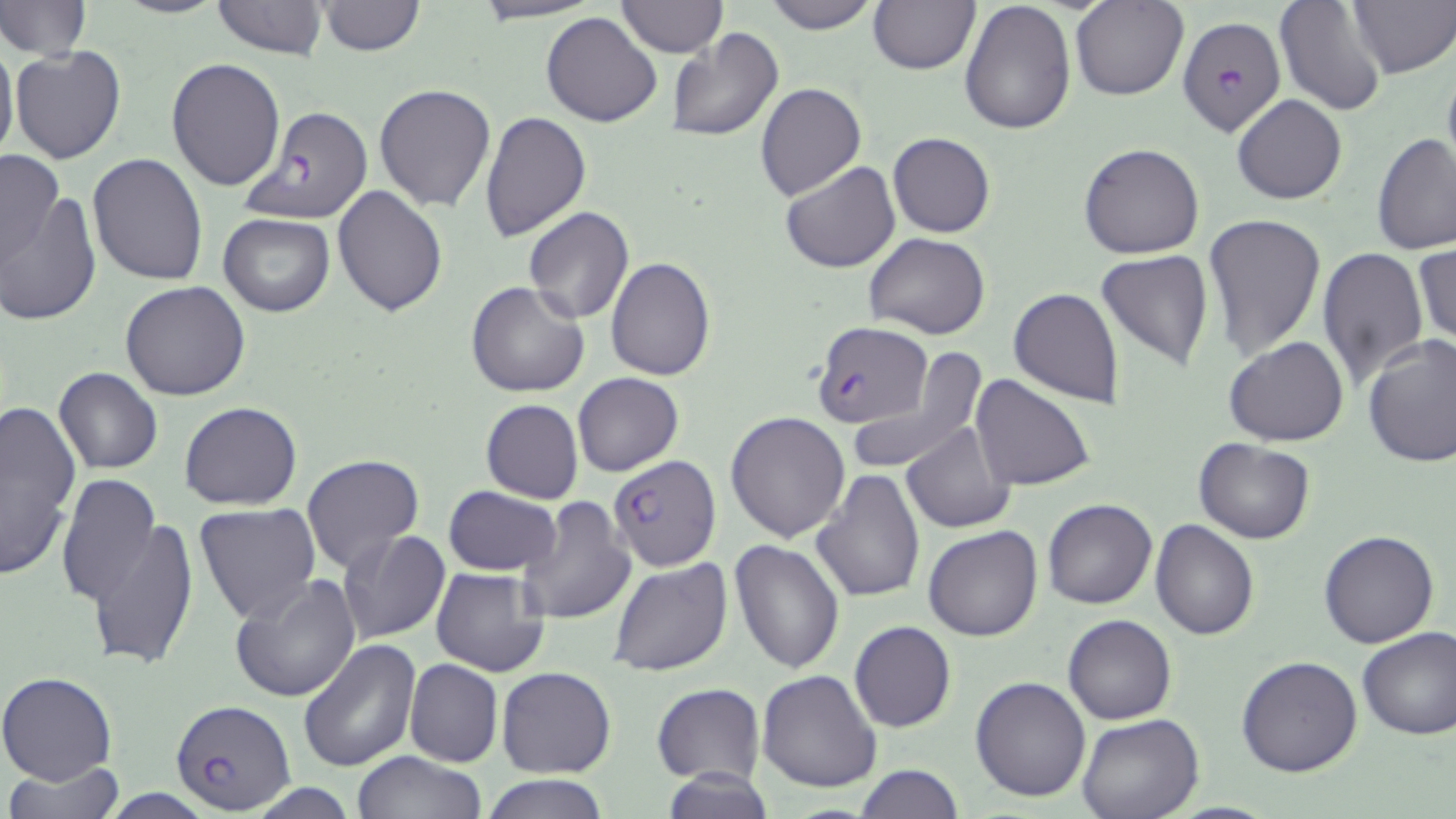
Approximate bounding boxes as named x1/y1/x2/y2 corners in pixels. Uninfected red blood cell locations: (x1=113, y1=0, x2=226, y2=20), (x1=210, y1=0, x2=329, y2=60), (x1=468, y1=0, x2=606, y2=24), (x1=614, y1=0, x2=727, y2=56), (x1=762, y1=0, x2=882, y2=33), (x1=958, y1=0, x2=1076, y2=136), (x1=1070, y1=0, x2=1188, y2=101), (x1=1274, y1=0, x2=1387, y2=117), (x1=1347, y1=0, x2=1456, y2=78), (x1=0, y1=1, x2=91, y2=62), (x1=316, y1=1, x2=425, y2=56), (x1=868, y1=1, x2=979, y2=74), (x1=542, y1=12, x2=664, y2=127), (x1=664, y1=28, x2=784, y2=143), (x1=0, y1=36, x2=18, y2=167), (x1=11, y1=46, x2=126, y2=165), (x1=167, y1=59, x2=287, y2=191), (x1=1442, y1=61, x2=1456, y2=178), (x1=373, y1=83, x2=496, y2=213), (x1=755, y1=83, x2=866, y2=200), (x1=1231, y1=94, x2=1347, y2=204), (x1=480, y1=113, x2=591, y2=243), (x1=888, y1=133, x2=995, y2=238), (x1=1373, y1=134, x2=1456, y2=256), (x1=1078, y1=142, x2=1204, y2=258), (x1=0, y1=148, x2=66, y2=269), (x1=88, y1=152, x2=209, y2=286), (x1=782, y1=160, x2=899, y2=273), (x1=2, y1=182, x2=102, y2=328), (x1=332, y1=187, x2=448, y2=316), (x1=523, y1=208, x2=634, y2=324), (x1=1201, y1=213, x2=1326, y2=360), (x1=218, y1=214, x2=335, y2=316), (x1=864, y1=232, x2=988, y2=340), (x1=1414, y1=242, x2=1455, y2=351), (x1=1315, y1=247, x2=1431, y2=387), (x1=1096, y1=249, x2=1215, y2=371), (x1=606, y1=256, x2=715, y2=380), (x1=120, y1=280, x2=252, y2=402), (x1=466, y1=281, x2=590, y2=397), (x1=1008, y1=286, x2=1127, y2=408), (x1=1362, y1=335, x2=1456, y2=468), (x1=1223, y1=337, x2=1349, y2=446), (x1=845, y1=348, x2=989, y2=477), (x1=53, y1=367, x2=162, y2=475), (x1=572, y1=373, x2=682, y2=476), (x1=970, y1=375, x2=1094, y2=492), (x1=0, y1=395, x2=81, y2=581), (x1=480, y1=399, x2=582, y2=504), (x1=179, y1=401, x2=303, y2=510), (x1=725, y1=411, x2=851, y2=543), (x1=901, y1=423, x2=1016, y2=532), (x1=1194, y1=437, x2=1316, y2=543), (x1=300, y1=454, x2=425, y2=576), (x1=812, y1=468, x2=925, y2=601), (x1=57, y1=473, x2=160, y2=607), (x1=443, y1=487, x2=562, y2=576), (x1=514, y1=495, x2=636, y2=625), (x1=1042, y1=498, x2=1157, y2=609), (x1=194, y1=503, x2=322, y2=626), (x1=87, y1=518, x2=201, y2=673), (x1=1151, y1=519, x2=1260, y2=639), (x1=922, y1=527, x2=1043, y2=642), (x1=1318, y1=528, x2=1440, y2=648), (x1=336, y1=529, x2=451, y2=645), (x1=729, y1=538, x2=845, y2=673), (x1=608, y1=558, x2=732, y2=678), (x1=430, y1=566, x2=554, y2=678), (x1=229, y1=575, x2=362, y2=703), (x1=1063, y1=614, x2=1177, y2=725), (x1=849, y1=621, x2=956, y2=732), (x1=1356, y1=625, x2=1455, y2=741), (x1=296, y1=639, x2=421, y2=773), (x1=1236, y1=655, x2=1363, y2=777), (x1=404, y1=659, x2=503, y2=767), (x1=496, y1=666, x2=616, y2=777), (x1=756, y1=669, x2=883, y2=793), (x1=0, y1=672, x2=118, y2=786), (x1=970, y1=676, x2=1091, y2=803), (x1=651, y1=683, x2=765, y2=786), (x1=1076, y1=711, x2=1203, y2=819), (x1=354, y1=750, x2=485, y2=819), (x1=3, y1=761, x2=126, y2=816), (x1=854, y1=764, x2=964, y2=819), (x1=656, y1=769, x2=776, y2=819), (x1=482, y1=772, x2=612, y2=818), (x1=243, y1=783, x2=361, y2=817). Plasmodium falciparum-infected red blood cell locations: (x1=1177, y1=14, x2=1287, y2=142), (x1=240, y1=105, x2=374, y2=225), (x1=813, y1=321, x2=930, y2=428), (x1=607, y1=455, x2=721, y2=573), (x1=171, y1=701, x2=294, y2=812). Slide-level diagnosis: Plasmodium falciparum. May-Grünwald-Giemsa-stained preparation. Thin blood film. 1000x magnification. Light microscopy. One field of a larger specimen. Image is 1456×819 pixels.